Locate every Plasmodium parasite.
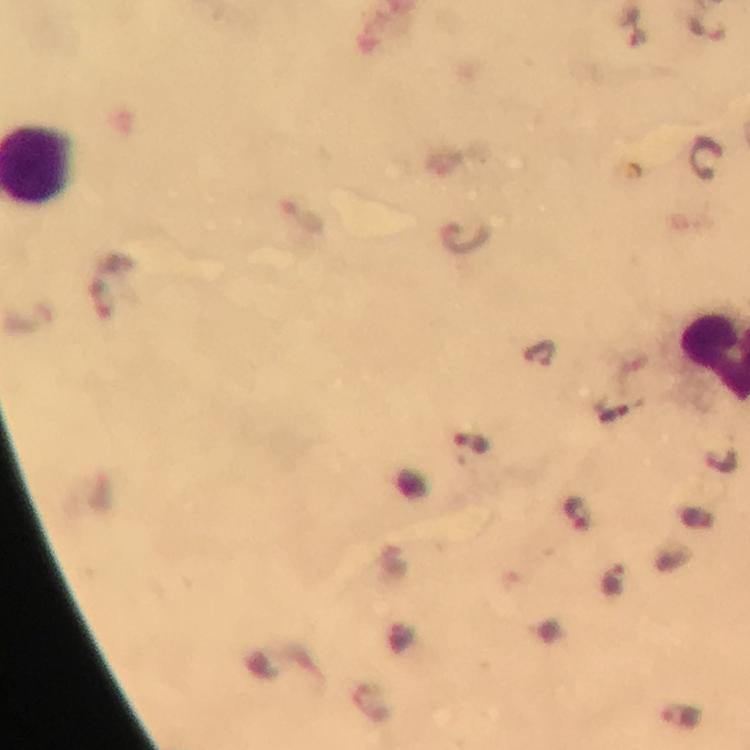

Approximate centers as [x, y] in pixels.
Plasmodium parasites: [704, 157], [301, 216], [465, 235], [538, 354], [613, 415], [469, 442], [578, 514], [613, 579], [681, 715].

Summary:
  - Preparation: thick smear
  - Magnification: 100x
  - Image size: 750×750 pixels
  - Immersion oil: used
  - Cropped from: a single field of view
  - Capture: smartphone photograph through a microscope
  - Context: from a malaria diagnostic workup
  - Stain: Giemsa